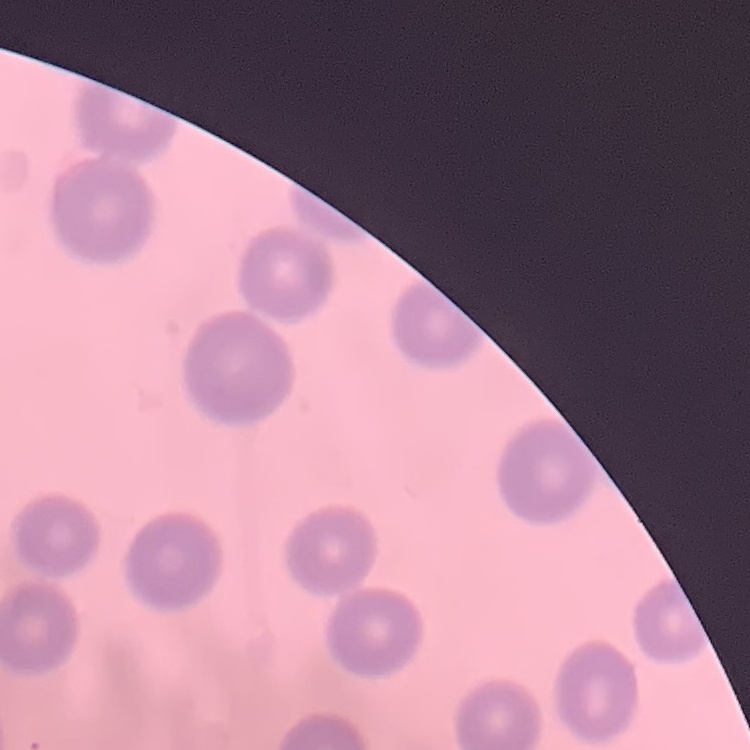
erythrocyte morphology = no rouleaux formation
image type = square crop of a larger photomicrograph
stain = Field's or Giemsa
preparation = thin peripheral smear